Locate every Plasmodium falciparum-infected red blood cell.
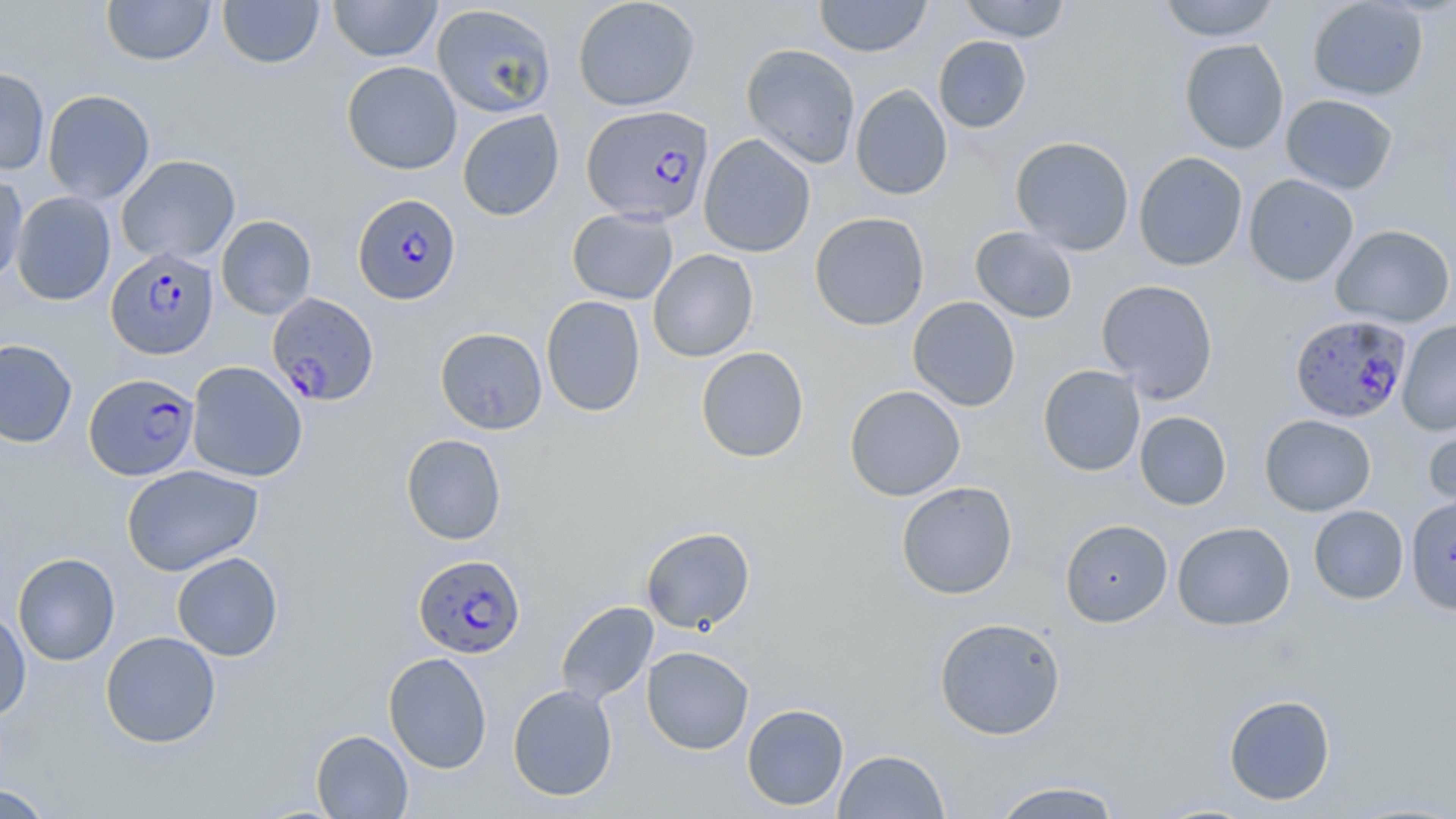

Approximate bounding boxes as (x1, y1, x2, y2) in pixels.
Plasmodium falciparum-infected red blood cells: (583, 106, 714, 226), (353, 194, 462, 305), (106, 248, 219, 360), (266, 292, 379, 406), (1290, 314, 1411, 423), (84, 373, 200, 480), (413, 554, 526, 659).

Summary:
  - Uninfected red blood cell locations: (101, 0, 216, 66), (217, 0, 325, 69), (328, 0, 442, 62), (572, 0, 700, 111), (814, 0, 932, 57), (958, 0, 1072, 42), (1158, 0, 1281, 41), (1307, 0, 1429, 101), (431, 4, 557, 118), (933, 35, 1032, 133), (1180, 38, 1289, 154), (740, 43, 861, 169), (341, 61, 462, 174), (0, 67, 50, 176), (850, 83, 952, 199), (42, 89, 155, 205), (1280, 93, 1399, 195), (457, 109, 565, 221), (698, 134, 816, 258), (1010, 136, 1135, 255), (1133, 151, 1248, 271), (116, 154, 240, 265), (0, 172, 28, 285), (1243, 174, 1359, 287), (11, 191, 116, 305), (567, 208, 678, 305), (809, 212, 930, 331), (216, 215, 317, 319), (1330, 224, 1455, 328), (970, 226, 1078, 323), (648, 249, 759, 362), (1096, 279, 1219, 402), (541, 295, 646, 417), (907, 296, 1021, 411), (1397, 319, 1456, 436), (435, 327, 547, 435), (0, 338, 78, 448), (696, 346, 809, 463), (186, 360, 308, 482), (1038, 365, 1145, 477), (844, 385, 966, 501), (1134, 410, 1232, 510), (1260, 414, 1376, 516), (1423, 415, 1456, 519), (400, 433, 507, 545), (122, 464, 264, 576), (896, 481, 1018, 599), (1405, 494, 1455, 616), (1308, 505, 1409, 604), (1059, 519, 1173, 628), (1172, 521, 1295, 631), (640, 526, 755, 634), (12, 552, 120, 666), (171, 552, 284, 661), (555, 600, 658, 707), (0, 606, 31, 722), (934, 616, 1066, 741), (100, 631, 221, 748), (641, 646, 754, 754), (383, 652, 492, 774), (507, 684, 618, 801), (1223, 694, 1335, 806), (742, 703, 849, 811), (311, 730, 413, 818), (833, 749, 950, 818), (989, 780, 1124, 819), (1, 783, 56, 818)
  - Slide-level diagnosis: Plasmodium falciparum
  - Preparation: thin blood smear
  - Image size: 1456×819 pixels
  - Field of view: single
  - Magnification: 1000x
  - Stain: May-Grünwald-Giemsa
  - Modality: light microscopy